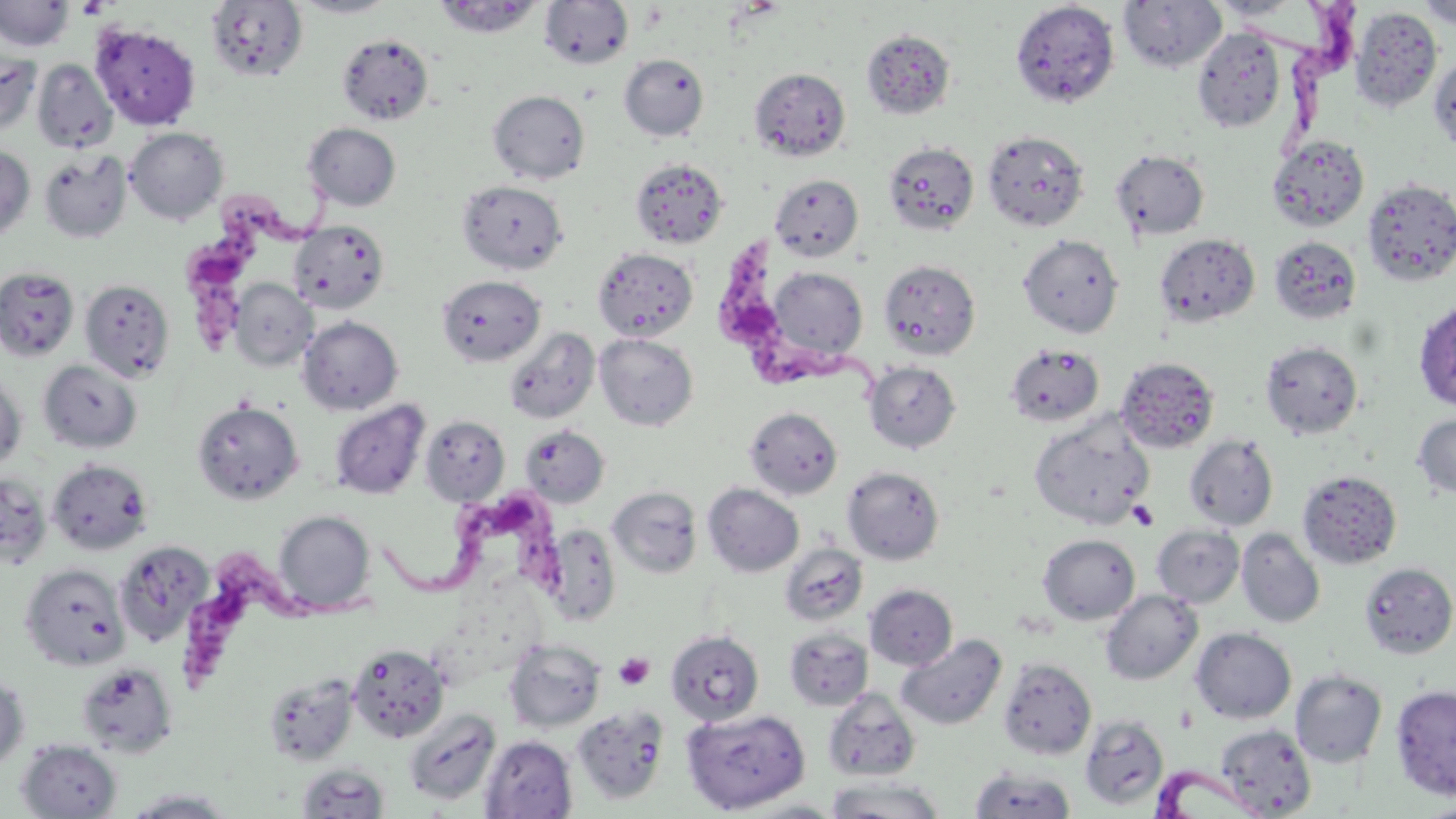
Approximate bounding boxes as [x1, y1, x2, y2] in pixels. Uninfected red blood cell locations: [289, 0, 400, 18], [432, 0, 546, 39], [1118, 0, 1227, 74], [1207, 0, 1312, 21], [1416, 0, 1456, 30], [0, 1, 74, 52], [205, 1, 308, 82], [539, 1, 634, 69], [1010, 2, 1120, 108], [1349, 6, 1442, 113], [90, 23, 201, 130], [1191, 28, 1287, 132], [860, 29, 956, 119], [336, 32, 434, 125], [0, 51, 41, 134], [619, 53, 709, 141], [1430, 54, 1456, 153], [33, 59, 117, 153], [749, 67, 851, 161], [488, 90, 590, 183], [303, 123, 401, 211], [125, 127, 228, 224], [982, 130, 1089, 232], [1267, 135, 1369, 232], [883, 141, 979, 234], [0, 146, 35, 241], [1111, 148, 1209, 240], [38, 150, 132, 243], [629, 157, 729, 249], [770, 174, 864, 262], [1362, 177, 1456, 287], [457, 179, 569, 274], [289, 220, 390, 314], [1154, 233, 1260, 328], [1018, 234, 1124, 338], [1269, 236, 1362, 325], [592, 247, 699, 342], [879, 259, 981, 360], [764, 266, 869, 366], [0, 267, 80, 361], [436, 274, 546, 367], [229, 278, 317, 371], [79, 279, 175, 382], [1414, 299, 1456, 412], [297, 316, 403, 415], [504, 327, 600, 424], [594, 333, 698, 431], [1260, 341, 1363, 439], [1004, 343, 1105, 427], [1116, 356, 1220, 453], [39, 359, 142, 453], [864, 361, 961, 453], [0, 373, 27, 471], [329, 399, 430, 499], [193, 400, 304, 504], [744, 406, 843, 500], [1412, 413, 1456, 499], [419, 414, 510, 505], [1029, 416, 1153, 527], [519, 425, 610, 507], [1184, 434, 1279, 531], [47, 459, 153, 555], [842, 466, 944, 564], [1298, 469, 1402, 569], [1, 472, 51, 570], [702, 483, 804, 577], [608, 486, 702, 578], [273, 510, 375, 614], [1151, 523, 1244, 608], [544, 525, 621, 624], [1237, 528, 1325, 628], [1038, 534, 1140, 625], [113, 541, 213, 647], [780, 543, 868, 627], [1359, 562, 1456, 659], [20, 564, 130, 671], [865, 583, 958, 671], [1100, 589, 1202, 685], [784, 627, 873, 711], [1191, 627, 1296, 724], [666, 629, 765, 725], [896, 634, 1007, 730], [503, 638, 606, 732], [347, 643, 449, 743], [997, 658, 1096, 760], [75, 662, 179, 757], [1290, 670, 1387, 768], [0, 672, 30, 772], [263, 673, 360, 766], [1391, 684, 1456, 801], [823, 688, 920, 781], [573, 706, 669, 806], [681, 708, 810, 814], [403, 709, 501, 806], [1079, 715, 1169, 811], [1216, 724, 1316, 817], [480, 735, 578, 819], [16, 738, 123, 819], [296, 763, 390, 818], [968, 767, 1077, 818], [825, 776, 945, 818], [123, 788, 238, 818], [733, 798, 849, 817], [1419, 799, 1456, 818]. Trypanosoma brucei locations: [1259, 0, 1362, 166], [186, 171, 340, 357], [719, 231, 890, 403], [385, 493, 582, 617], [178, 541, 375, 700], [1152, 766, 1268, 818]. Platelet locations: [77, 1, 110, 18], [1128, 501, 1158, 531], [614, 652, 654, 690]. Slide-level diagnosis: Trypanosoma brucei. Light microscopy. Captured at 1000x magnification. One field of a larger specimen. Thin blood film. Image is 1456×819 pixels. May-Grünwald-Giemsa-stained preparation.